Classify this cell by malaria status.
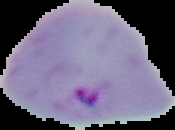

Parasitized.

The area outside the segmented cell region is set to black. Image is 175×130 pixels. From a thin blood smear.